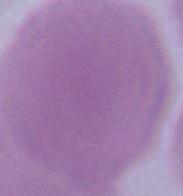

modality = photomicrograph
identification = erythrocyte
magnification = 1000x